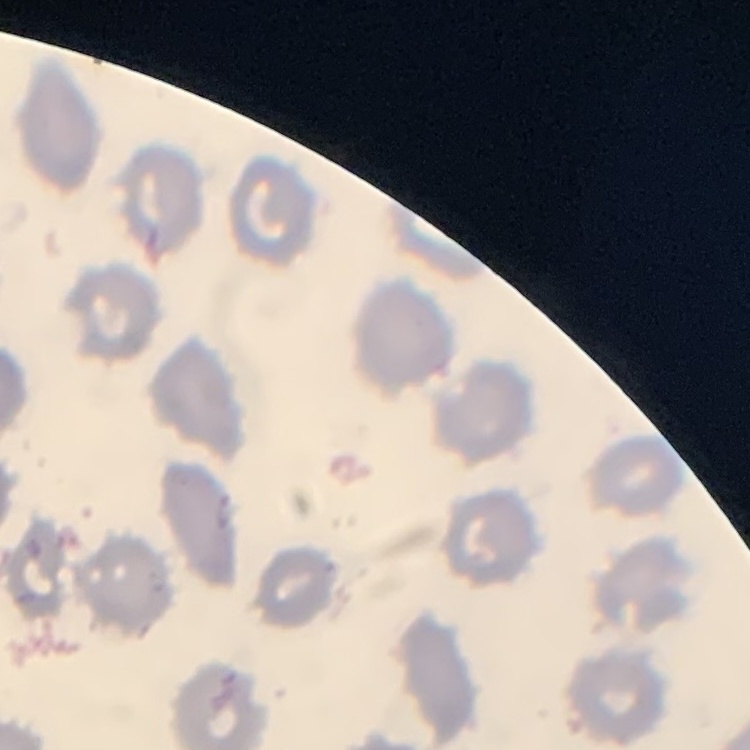
red blood cell morphology = no rouleaux formation
stain = Field's or Giemsa
preparation = thin blood smear
image type = square crop of a larger photomicrograph